State which cell type is depicted.
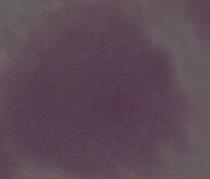

An erythrocyte.

Photomicrograph. 1000x magnification.